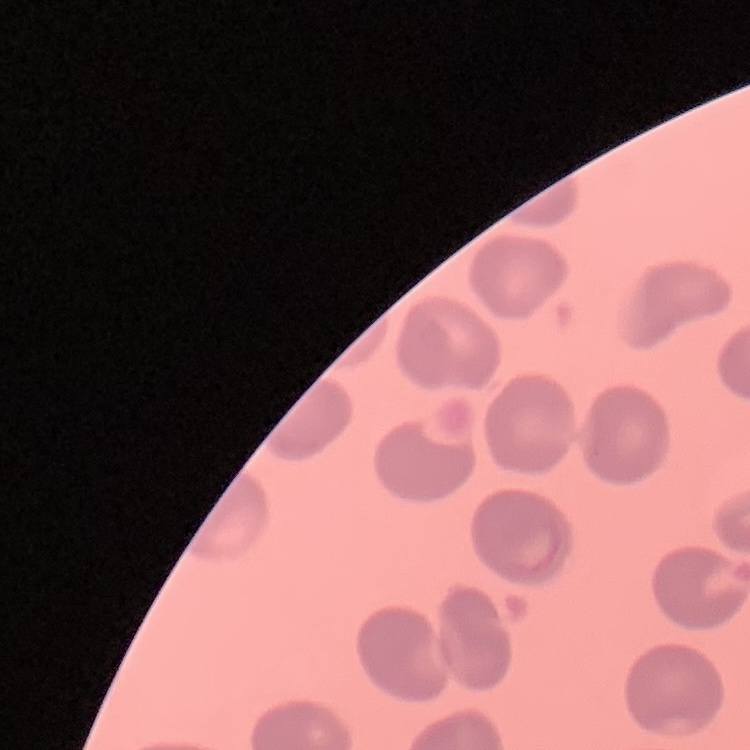

erythrocyte morphology = no rouleaux formation
image type = one tile cut from a larger photomicrograph
stain = Field's or Giemsa
preparation = thin peripheral smear